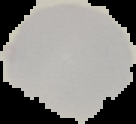
Cell region segmented out of the field of view; the surrounding area is masked to black. Result: no malaria parasites detected. From a thin blood film. Image is 136×124 pixels.